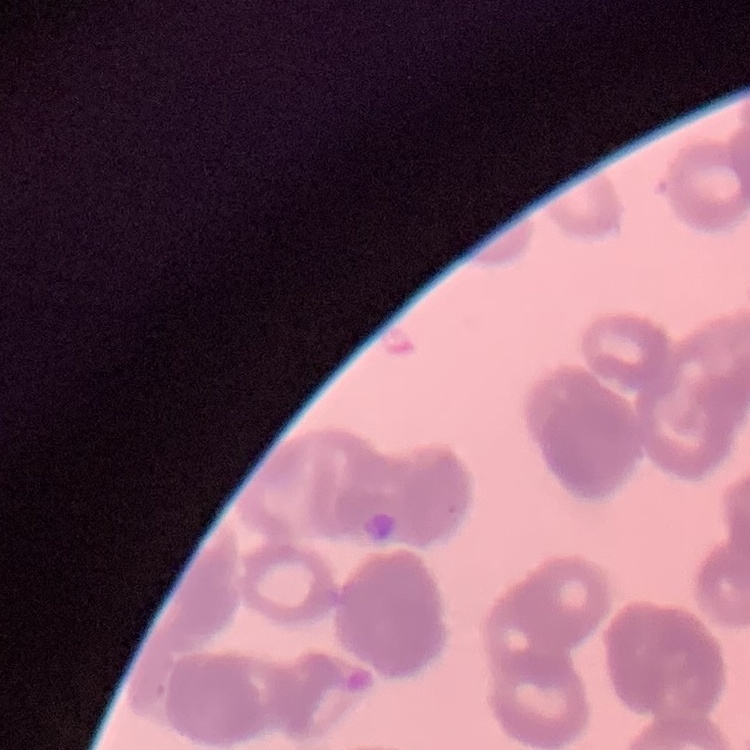

The red blood cells show rouleaux formation. One tile cut from a larger photomicrograph. Thin blood film. Stained with either Field's or Giemsa.